Name the parasite shown.
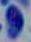
Toxoplasma gondii.

magnification = 1000x
modality = micrograph